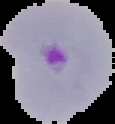
Malaria status: parasitized. From a thin blood smear. Image is 115×124 pixels. Cell region segmented out of the field of view; the surrounding area is masked to black.